Report the malaria status of this cell.
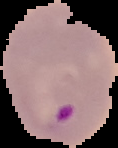

Parasitized.

image type = segmented cell region with the area outside set to black
image size = 118×148 pixels
preparation = thin blood film